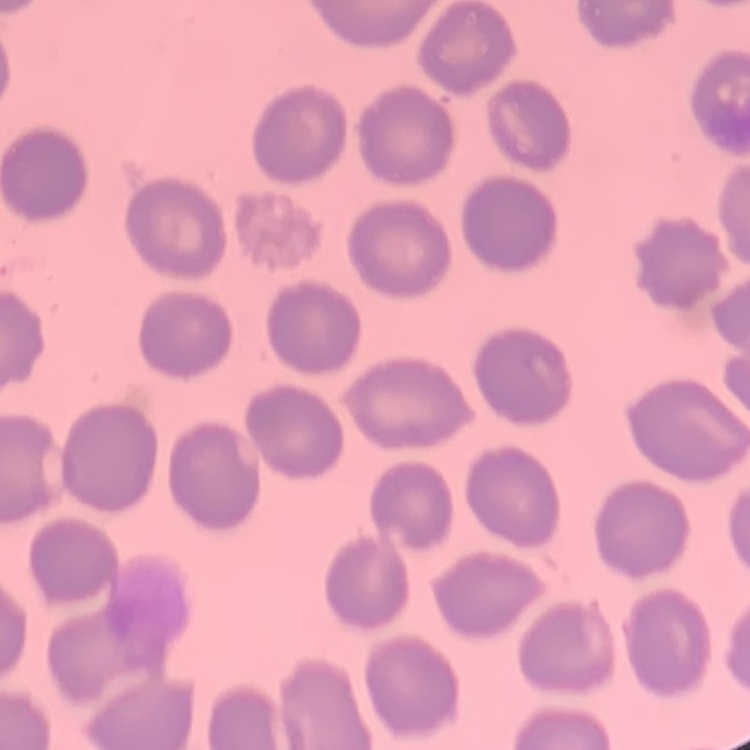
The erythrocytes show no rouleaux formation. Square crop of a larger photomicrograph. Stained with either Field's or Giemsa. Thin peripheral smear.